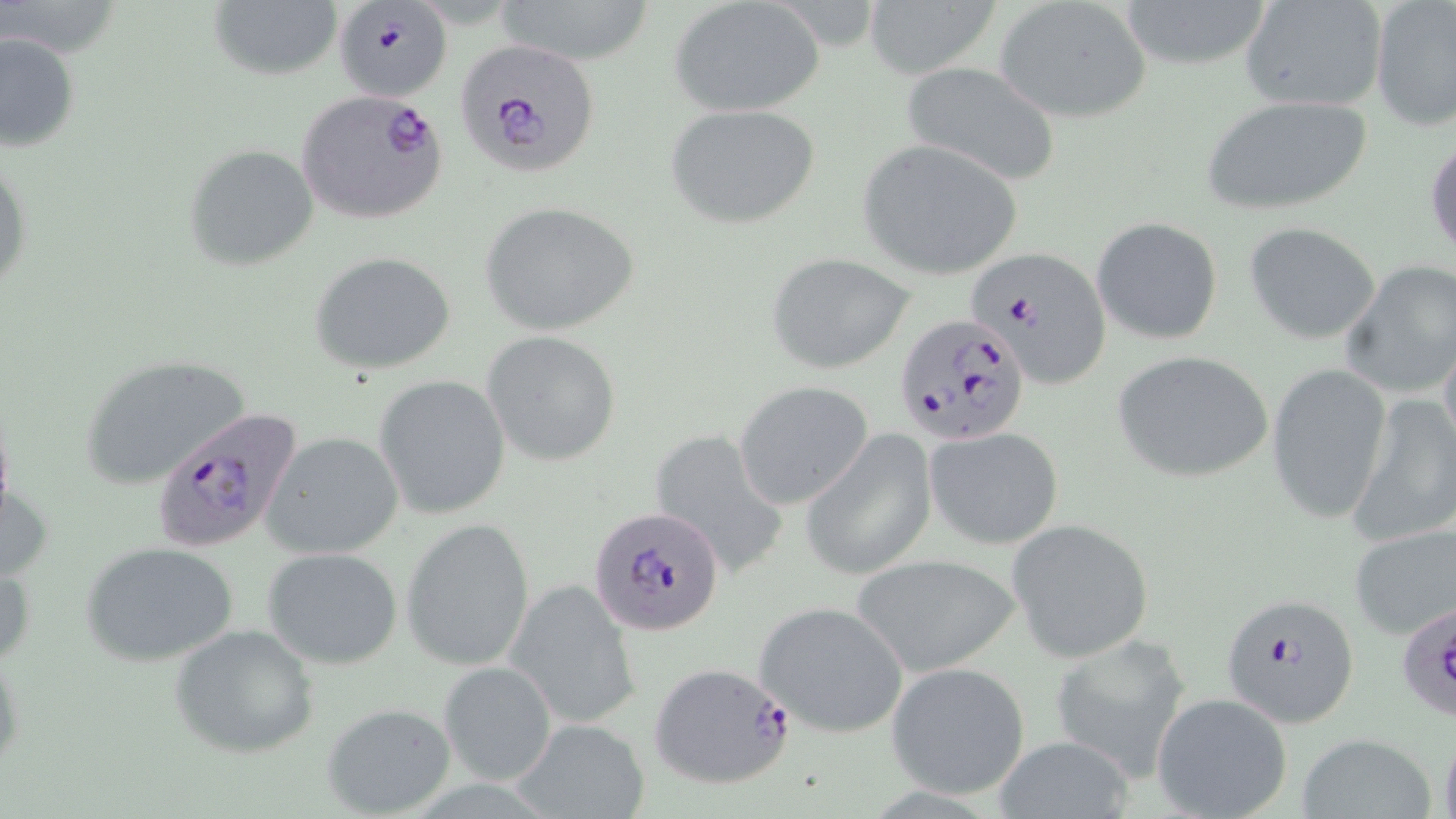 Approximate bounding boxes as (x1,y1)-(x2,y2) corner pairs in pixels. Plasmodium falciparum-infected red blood cell locations: (335,5)-(456,109), (452,37)-(601,177), (297,89)-(448,224), (969,246)-(1112,388), (897,313)-(1030,446), (147,406)-(304,552), (592,504)-(725,636), (1223,593)-(1361,727), (1397,593)-(1456,723), (649,661)-(796,790). Uninfected red blood cell locations: (490,0)-(661,66), (1113,0)-(1276,70), (1240,0)-(1389,114), (1370,0)-(1456,132), (207,1)-(341,81), (669,1)-(824,119), (861,1)-(996,77), (993,2)-(1153,125), (0,30)-(81,156), (900,61)-(1062,188), (1198,94)-(1373,217), (666,103)-(821,230), (1427,137)-(1456,264), (856,141)-(1024,279), (183,144)-(319,271), (0,147)-(33,303), (479,201)-(640,337), (1090,216)-(1222,345), (1244,221)-(1381,345), (311,250)-(458,377), (767,253)-(917,374), (1340,259)-(1456,398), (1438,328)-(1456,461), (481,330)-(623,467), (1112,350)-(1273,483), (82,354)-(253,490), (1265,362)-(1392,525), (374,374)-(511,519), (734,382)-(873,508), (1349,392)-(1456,547), (924,426)-(1064,550), (650,429)-(790,581), (800,430)-(937,580), (262,432)-(404,559), (401,517)-(535,672), (1008,519)-(1154,663), (1348,521)-(1456,641), (81,541)-(239,668), (263,547)-(404,669), (851,553)-(1023,677), (506,580)-(640,729), (755,601)-(909,738), (169,623)-(320,759), (1047,630)-(1193,780), (0,642)-(24,778), (436,661)-(557,787), (885,661)-(1031,799), (1151,693)-(1292,819), (322,702)-(456,817), (504,717)-(652,819), (1297,732)-(1436,817), (992,738)-(1135,816). Slide-level diagnosis: Plasmodium falciparum. Captured at 1000x magnification. May-Grünwald-Giemsa stain. Thin blood smear. Image is 1456×819 pixels. Light microscopy. One field of a larger specimen.